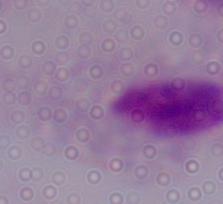
Summary:
  - Modality: micrograph
  - Magnification: 1000x
  - Identification: trichomonad